Give the position of every Plasmodium parasite visible.
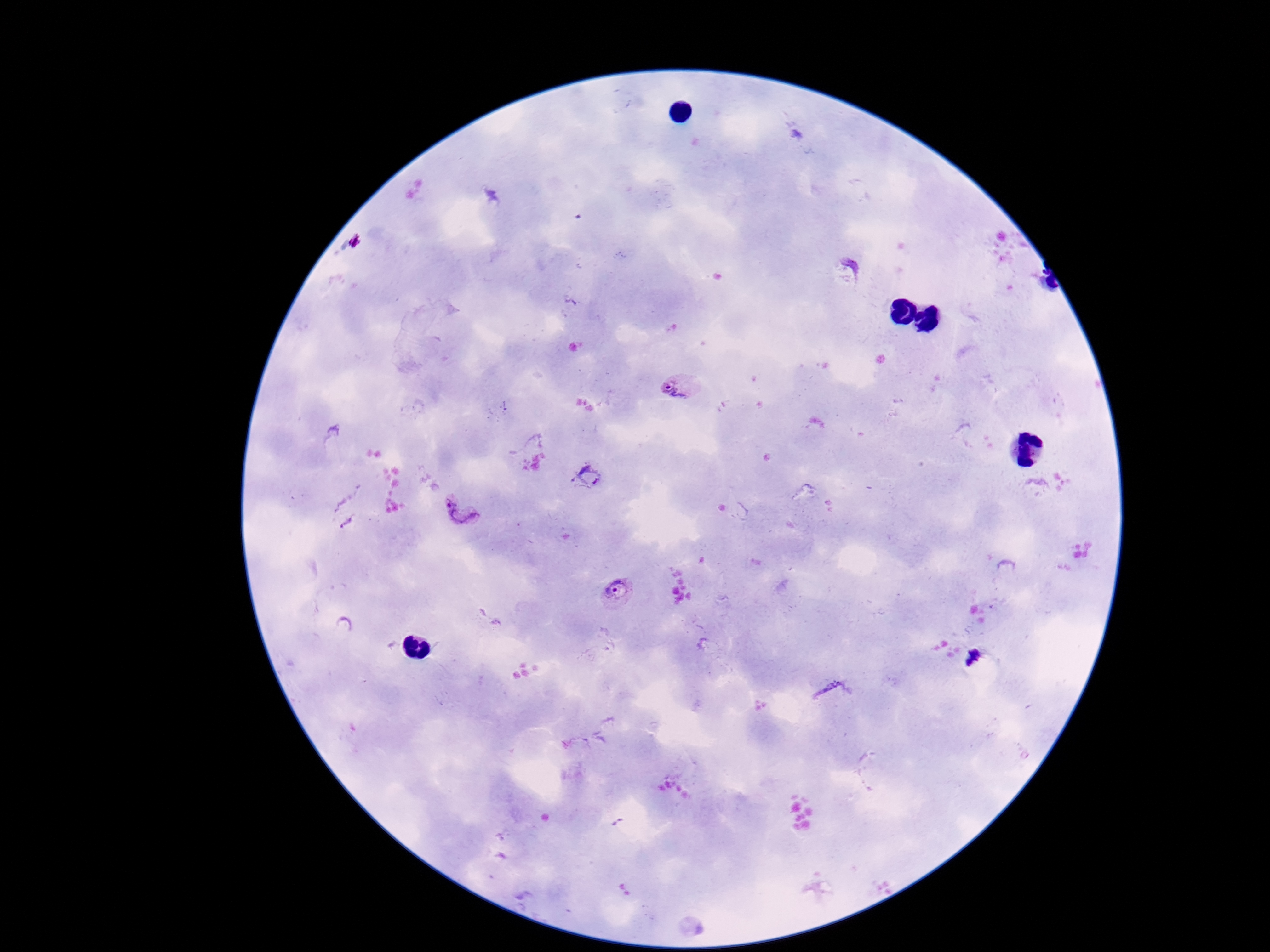
Approximate centers as [x, y] in pixels.
Plasmodium parasites: [357, 241], [681, 387], [499, 410], [589, 476], [344, 509], [461, 511], [618, 592], [975, 661], [834, 693].

image size = 1270×952 pixels
field of view = one from this slide
magnification = 100x
patient malaria status = infected
preparation = thick blood smear
stain = Giemsa
capture = smartphone camera through the microscope eyepiece